Assess the morphology of the erythrocytes.
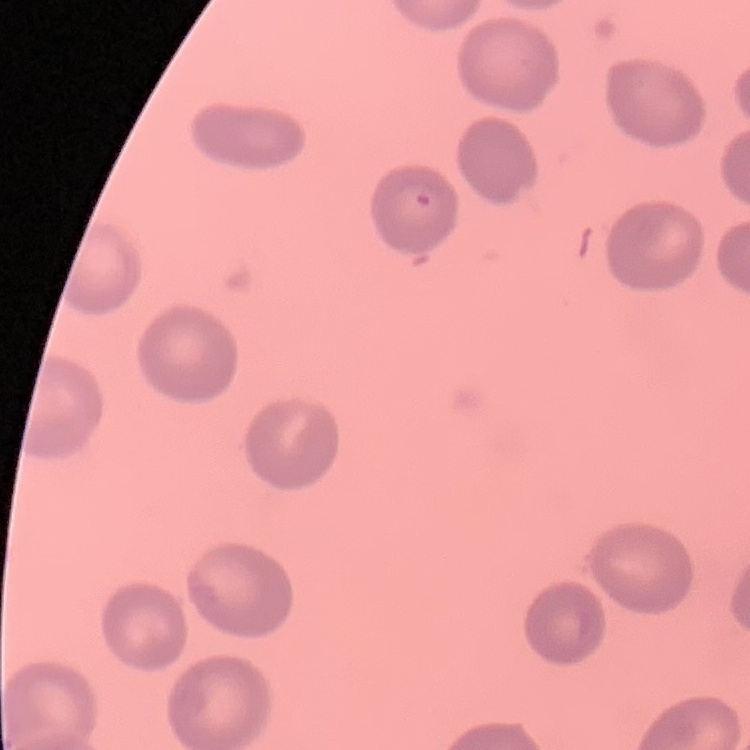
They show no rouleaux formation.

Field's or Giemsa stain. Thin peripheral smear. One tile cut from a larger photomicrograph.